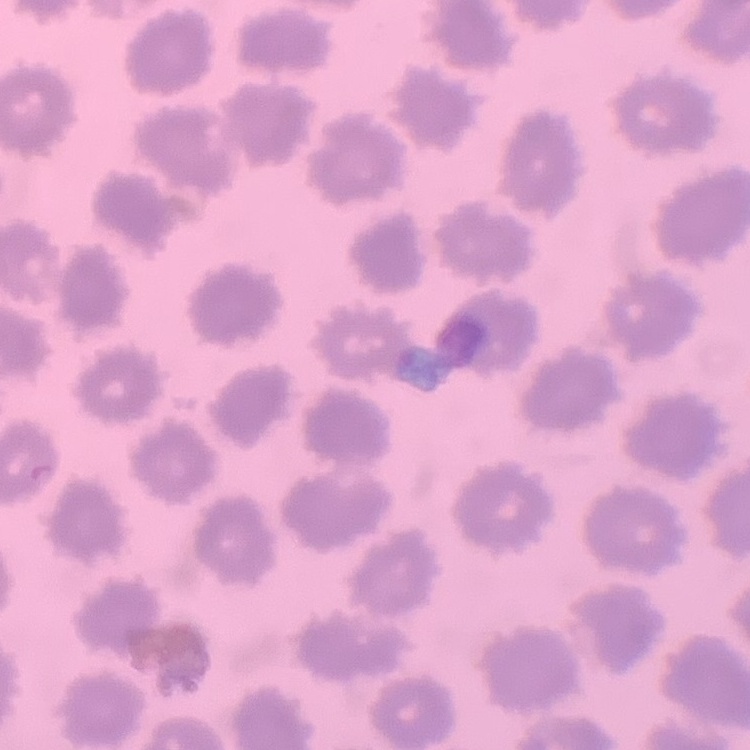
The red blood cells show no rouleaux formation. Stained with either Field's or Giemsa. Thin blood smear. One tile cut from a larger photomicrograph.